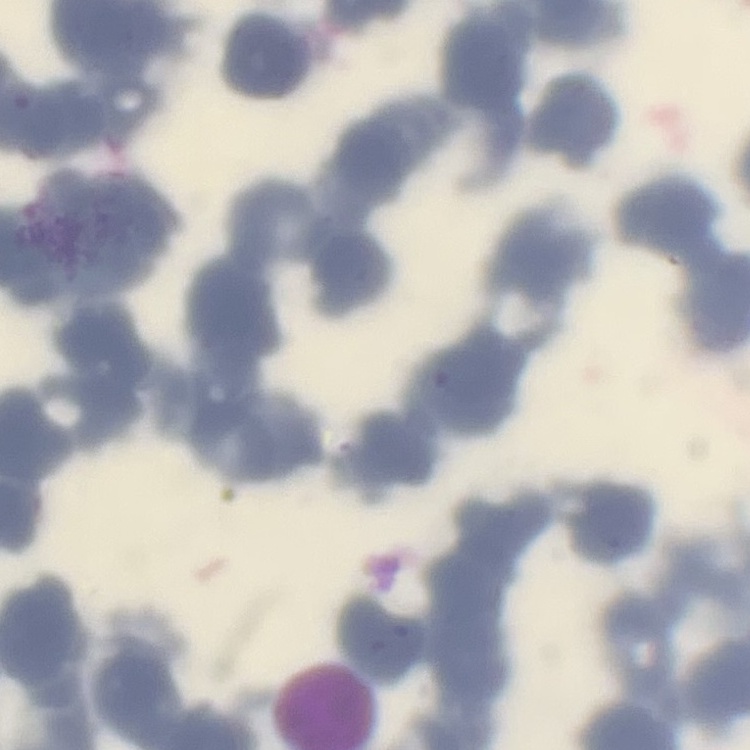

Summary:
  - Erythrocyte morphology: rouleaux formation
  - Preparation: thin peripheral smear
  - Image type: one tile cut from a larger photomicrograph
  - Stain: Field's or Giemsa